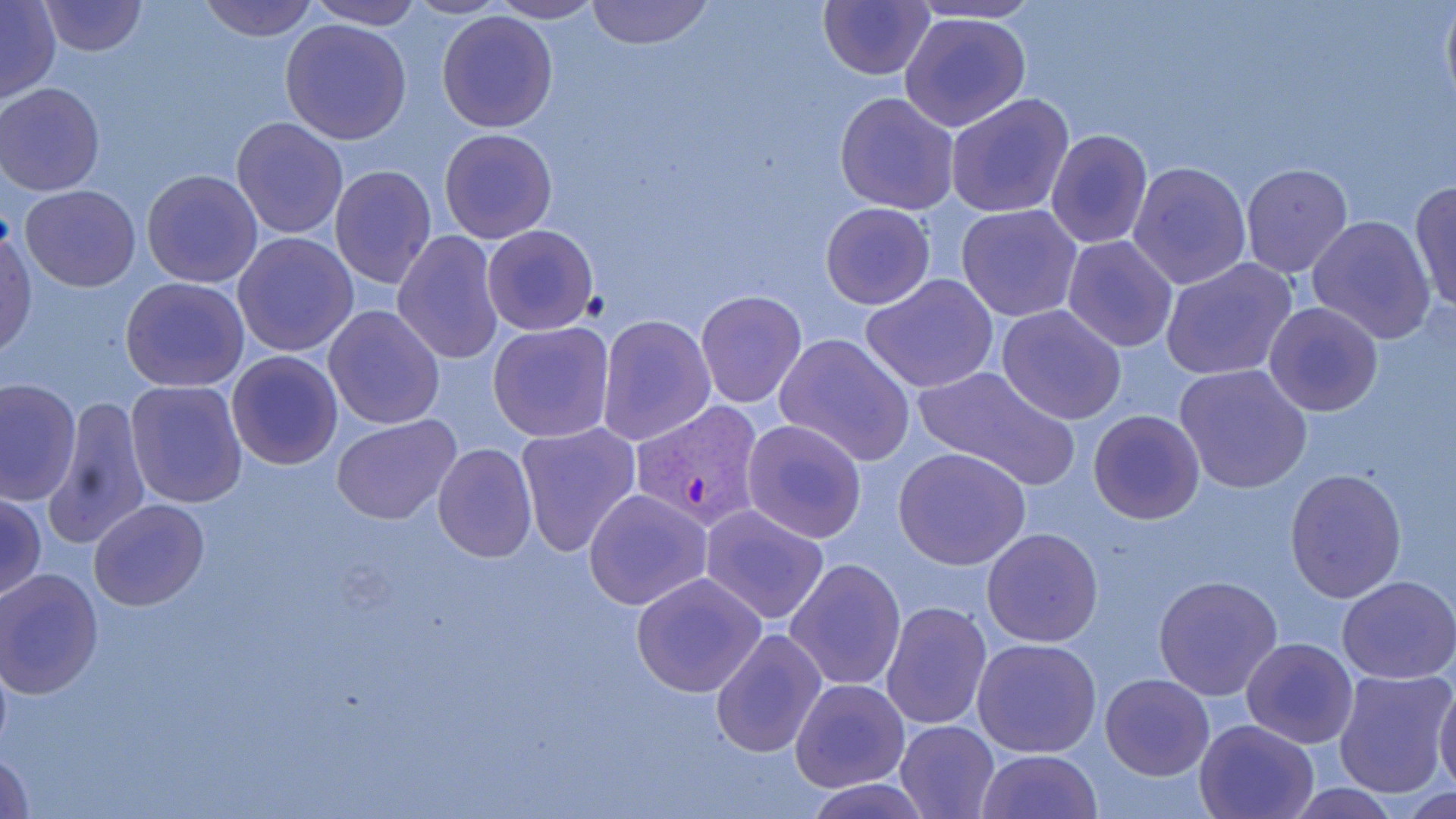
Summary:
  - Coordinate format: approximate bounding boxes as [x1, y1, x2, y2] in pixels
  - Plasmodium vivax-infected red blood cell locations: [631, 400, 766, 529]
  - Uninfected red blood cell locations: [38, 0, 147, 55], [197, 0, 320, 41], [401, 0, 511, 20], [585, 0, 713, 49], [819, 0, 936, 79], [1440, 0, 1455, 120], [307, 1, 424, 29], [488, 1, 605, 24], [898, 1, 1052, 26], [1, 2, 60, 103], [435, 9, 559, 132], [900, 10, 1031, 132], [280, 19, 411, 144], [1, 83, 105, 196], [834, 91, 960, 214], [945, 93, 1076, 220], [230, 116, 349, 239], [438, 127, 557, 243], [1045, 128, 1153, 251], [1128, 160, 1252, 291], [328, 164, 437, 288], [1239, 164, 1354, 280], [141, 169, 263, 287], [1409, 181, 1456, 315], [19, 184, 140, 291], [821, 202, 935, 311], [956, 203, 1082, 322], [1305, 213, 1437, 345], [482, 224, 599, 335], [0, 228, 36, 355], [391, 230, 503, 367], [233, 231, 359, 358], [1062, 235, 1177, 352], [1159, 258, 1296, 382], [860, 273, 999, 393], [119, 275, 250, 393], [696, 291, 805, 407], [1262, 302, 1385, 417], [323, 304, 447, 430], [996, 304, 1129, 425], [595, 313, 716, 447], [487, 320, 617, 444], [774, 332, 915, 466], [226, 350, 343, 470], [913, 365, 1080, 491], [1174, 365, 1314, 497], [0, 376, 82, 507], [124, 378, 248, 508], [46, 396, 151, 550], [1089, 409, 1205, 525], [331, 415, 461, 525], [741, 418, 867, 543], [514, 422, 641, 560], [432, 443, 536, 563], [893, 447, 1031, 570], [1284, 467, 1407, 603], [584, 488, 712, 611], [0, 490, 47, 603], [88, 499, 209, 611], [700, 505, 831, 625], [981, 528, 1104, 648], [785, 558, 906, 691], [0, 568, 103, 699], [630, 571, 769, 697], [1153, 573, 1283, 702], [1338, 575, 1456, 684], [881, 600, 993, 732], [710, 627, 828, 760], [972, 637, 1102, 757], [1242, 637, 1357, 748], [1331, 668, 1455, 800], [1101, 673, 1213, 781], [791, 678, 909, 791], [1434, 679, 1456, 799], [1195, 718, 1318, 818], [894, 720, 1001, 819], [0, 746, 36, 819], [978, 749, 1102, 819], [801, 778, 933, 818]
  - Slide-level diagnosis: Plasmodium vivax
  - Preparation: thin blood film
  - Magnification: 1000x
  - Stain: May-Grünwald-Giemsa
  - Field of view: single
  - Image size: 1456×819 pixels
  - Modality: light microscopy